Assess the morphology of the erythrocytes.
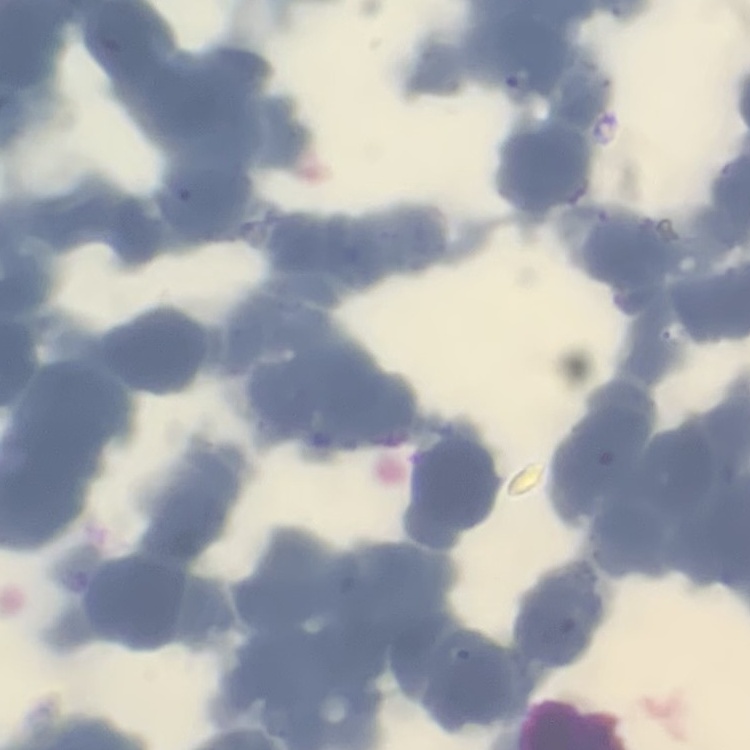
They show rouleaux formation.

stain = Field's or Giemsa
image type = square crop of a larger photomicrograph
preparation = thin blood film